Assess this cell for malaria.
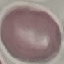

It is uninfected.

capture: smartphone through the microscope eyepiece
preparation: thin blood smear
image_type: cell patch, automatically extracted from a larger field of view and resized to 64 × 64 pixels
stain: Giemsa